Identify the parasite.
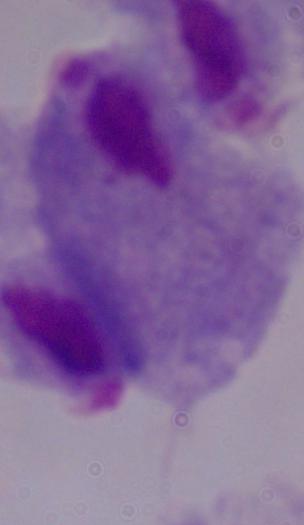

A trichomonad.

Summary:
  - Modality: micrograph
  - Magnification: 1000x